Give a bounding box for every Plasmodium parasite.
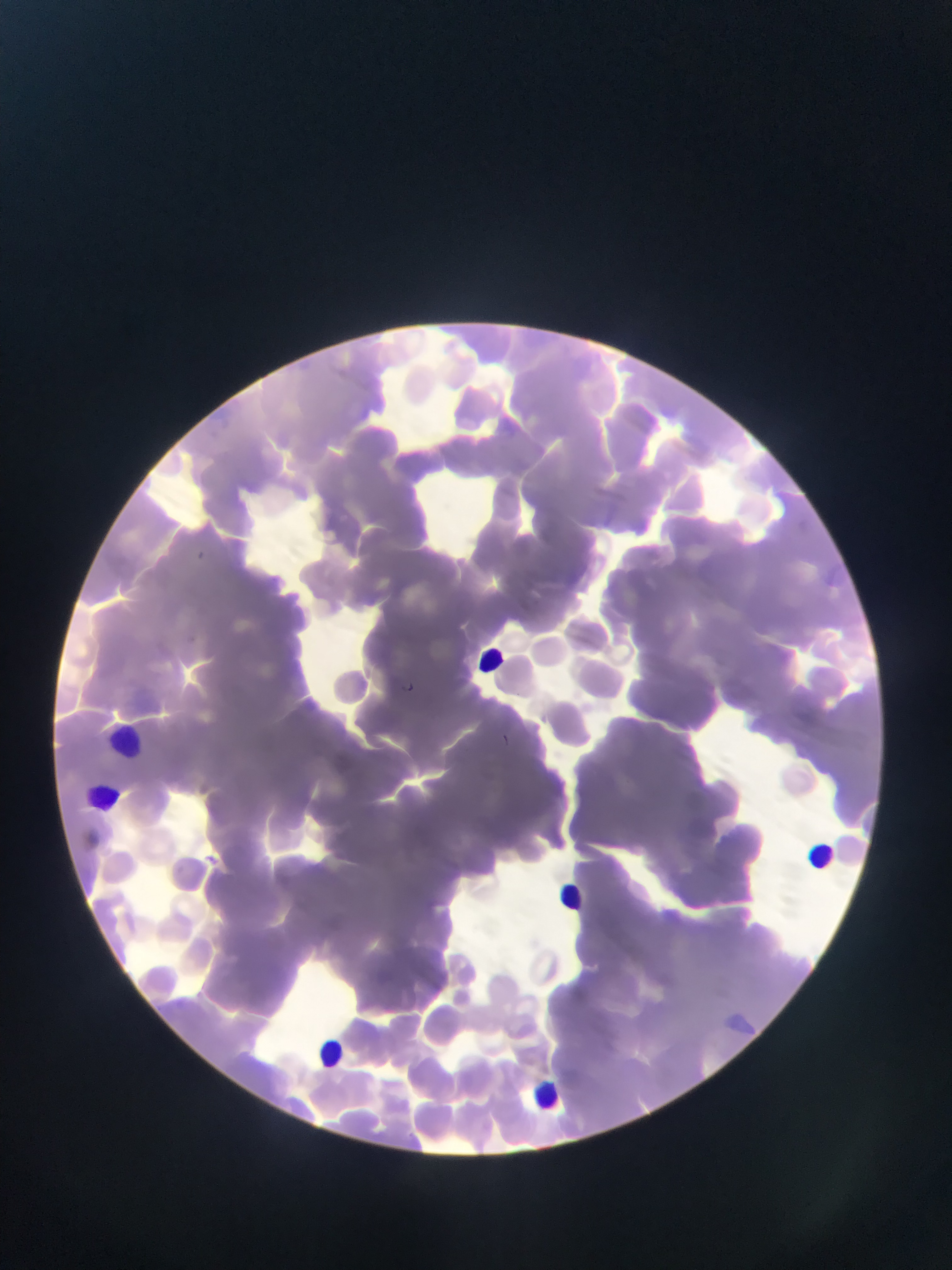

Approximate bounding boxes as (left, top, right, bottom) in pixels.
Plasmodium parasites: (196, 547, 208, 557), (400, 678, 420, 697), (497, 733, 522, 744).

country = Ghana
leukocyte locations = approximate bounding boxes as (left, top, right, bottom) in pixels: (472, 639, 507, 674), (104, 724, 146, 756), (77, 776, 114, 818), (805, 841, 836, 873), (551, 868, 583, 914), (316, 1033, 357, 1064), (518, 1074, 569, 1122)
field of view = single
capture = mobile-phone photograph through a microscope
image size = 952×1270 pixels
preparation = thin blood smear